Comment on the morphology of the red blood cells.
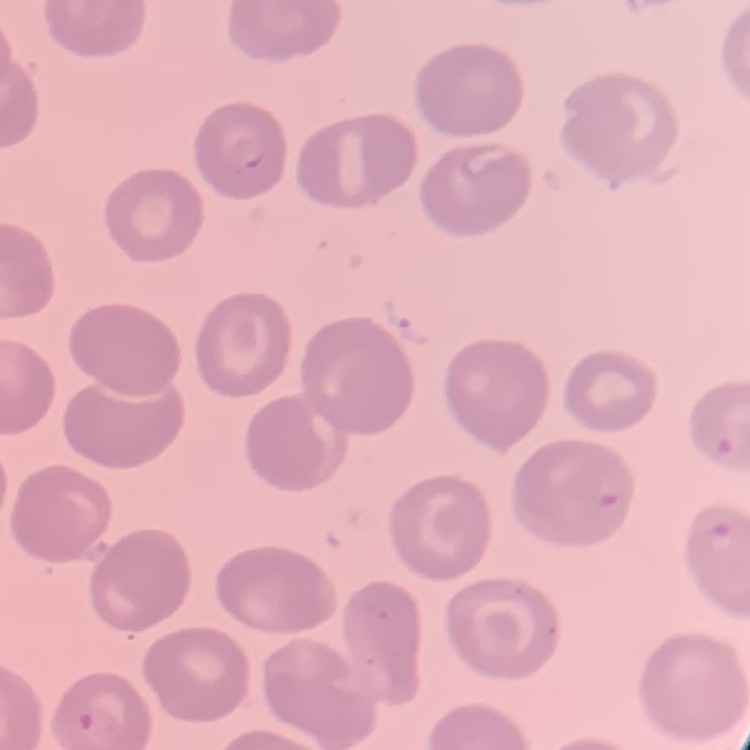
They show no rouleaux formation.

Summary:
  - Preparation: thin blood film
  - Stain: Field's or Giemsa
  - Image type: one tile cut from a larger photomicrograph